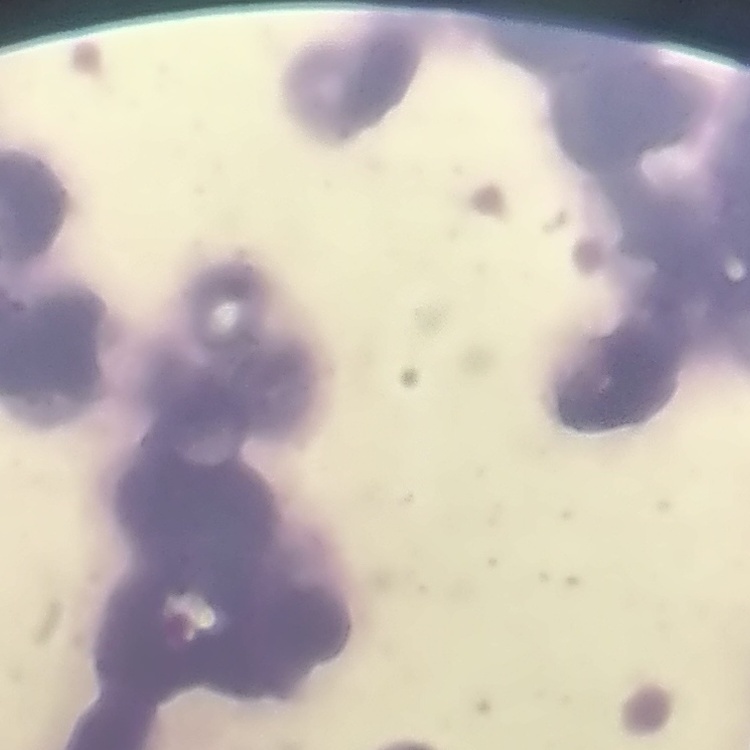

Summary:
  - Red blood cell morphology: rouleaux formation
  - Stain: Field's or Giemsa
  - Preparation: thin peripheral smear
  - Image type: square crop of a larger photomicrograph